Name the parasite shown.
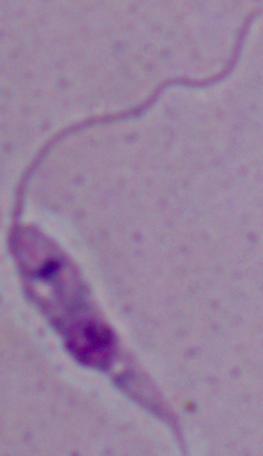

Leishmania.

1000x magnification. Micrograph.